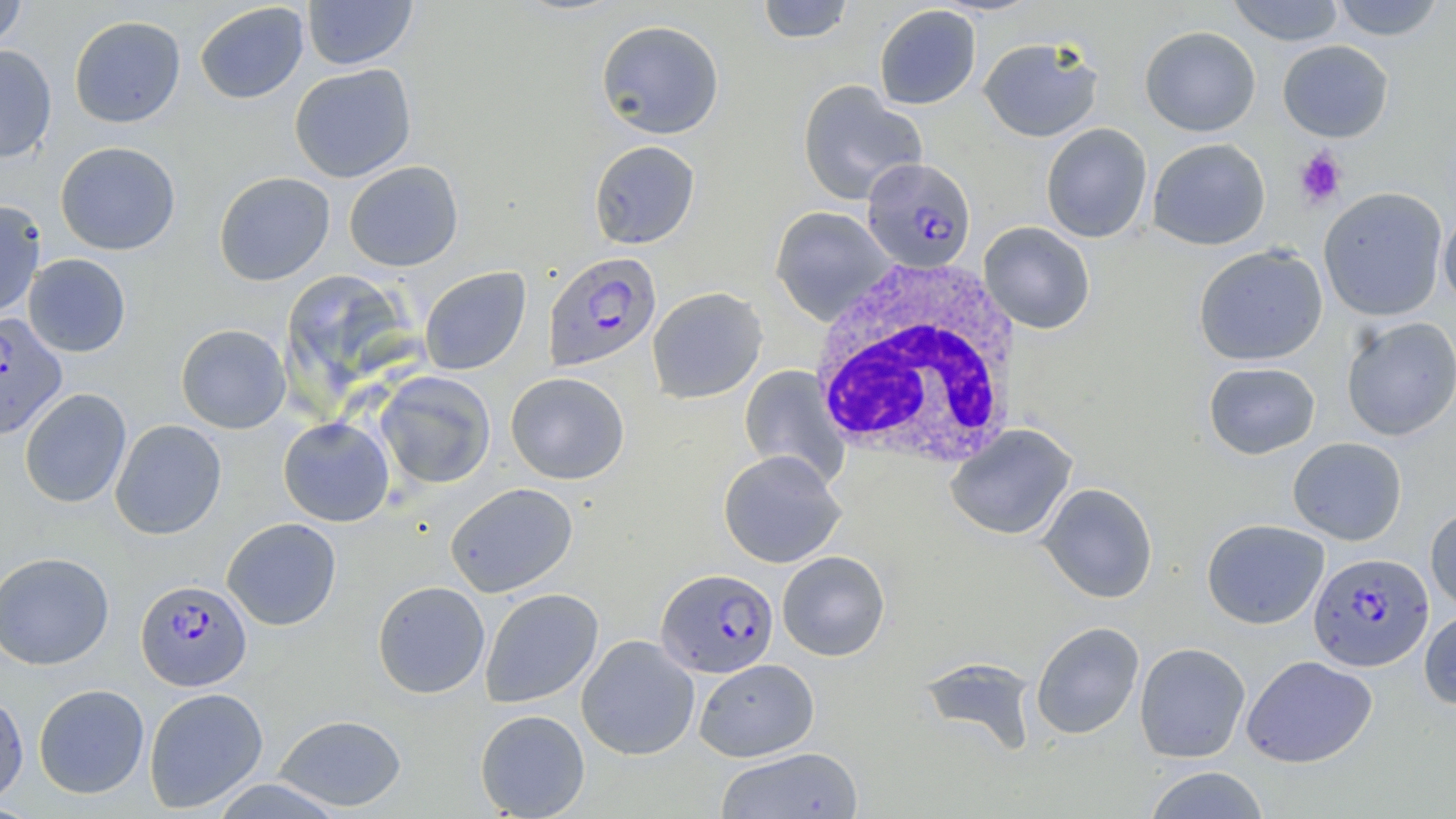
Approximate bounding boxes as [x1, y1, x2, y2] in pixels. Plasmodium falciparum-infected red blood cell locations: [862, 157, 976, 273], [543, 252, 661, 371], [0, 312, 67, 441], [1308, 552, 1433, 671], [656, 568, 779, 677], [136, 579, 252, 691]. Uninfected red blood cell locations: [0, 0, 27, 53], [302, 0, 417, 70], [1227, 0, 1344, 46], [1331, 0, 1446, 41], [757, 1, 855, 43], [194, 2, 309, 104], [874, 5, 981, 110], [69, 15, 186, 128], [596, 19, 725, 140], [1140, 25, 1261, 136], [978, 36, 1103, 142], [1278, 40, 1394, 142], [0, 44, 57, 163], [289, 64, 417, 183], [797, 80, 927, 204], [1041, 123, 1153, 243], [1147, 138, 1270, 250], [589, 140, 700, 249], [55, 141, 181, 255], [343, 160, 464, 272], [213, 171, 335, 286], [1318, 187, 1448, 321], [0, 199, 46, 321], [770, 207, 895, 325], [1438, 209, 1456, 310], [978, 221, 1095, 334], [1193, 244, 1328, 366], [23, 253, 131, 357], [420, 267, 531, 375], [647, 286, 767, 404], [1340, 317, 1456, 441], [175, 324, 291, 433], [1203, 361, 1320, 459], [739, 365, 849, 486], [375, 371, 496, 489], [505, 371, 630, 484], [19, 388, 132, 509], [278, 417, 395, 527], [110, 419, 227, 540], [945, 424, 1077, 541], [1288, 437, 1407, 545], [718, 450, 846, 568], [444, 482, 578, 598], [1038, 482, 1158, 603], [1425, 505, 1456, 614], [222, 517, 342, 630], [1201, 519, 1329, 629], [777, 551, 890, 661], [0, 552, 114, 670], [372, 580, 490, 698], [480, 588, 603, 709], [1419, 608, 1456, 709], [1030, 622, 1144, 740], [576, 635, 700, 760], [1134, 642, 1250, 763], [1241, 655, 1377, 768], [919, 656, 1040, 756], [694, 658, 819, 762], [33, 683, 149, 799], [143, 687, 269, 813], [0, 689, 29, 805], [475, 709, 590, 818], [273, 714, 408, 812], [714, 747, 864, 819], [1143, 766, 1270, 819]. White blood cell locations: [806, 258, 1023, 471]. Platelet locations: [1294, 147, 1347, 208]. Slide-level diagnosis: Plasmodium falciparum. One field of a larger specimen. Thin blood film. Image is 1456×819 pixels. Captured at 1000x magnification. May-Grünwald-Giemsa stain. Optical microscopy.